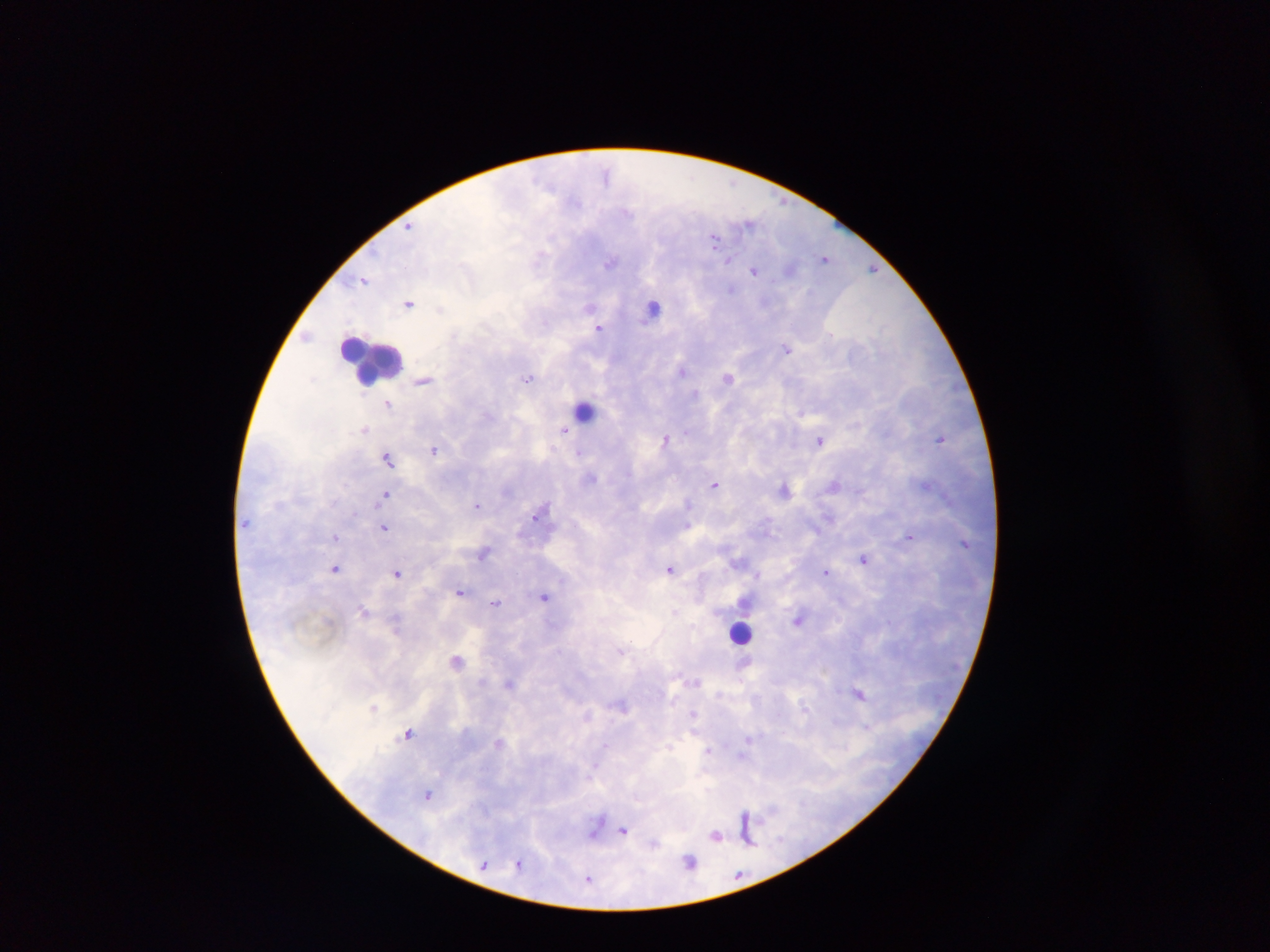

leukocyte_locations: 'approximate centers as [x, y] in pixels: [651, 308], [370, 359], [585, 409], [740, 632]'
malaria_parasite_locations: 'approximate centers as [x, y] in pixels: [605, 173], [783, 202], [626, 211], [748, 224], [410, 225], [714, 237], [824, 258], [729, 260], [611, 263], [873, 268], [753, 271], [364, 280], [730, 288], [409, 304], [590, 307], [441, 309], [599, 329], [787, 348], [682, 371], [529, 377], [728, 378], [423, 381], [695, 393], [388, 403], [365, 429], [565, 430], [940, 438], [665, 439], [821, 440], [434, 449], [579, 452], [387, 458], [591, 477], [714, 484], [833, 484], [785, 489], [385, 494], [688, 503], [476, 505], [541, 511], [354, 514], [384, 527], [909, 536], [335, 537], [483, 553], [864, 559], [738, 561], [335, 568], [670, 569], [826, 572], [397, 573], [757, 575], [461, 591], [545, 597], [495, 603], [364, 611], [675, 611], [798, 620], [622, 650], [458, 660], [744, 665], [509, 684], [859, 694], [621, 704], [693, 714], [588, 716], [408, 733], [747, 739], [499, 742], [604, 744], [708, 749], [742, 756], [594, 767], [429, 794], [745, 816], [624, 831], [716, 835], [749, 843], [690, 861], [519, 863], [484, 864], [739, 875], [588, 879]'
country: Ghana
field_of_view: single
preparation: thick blood film
image_size: 1270×952 pixels
capture: mobile-phone photograph through a microscope